Report the malaria status of this cell.
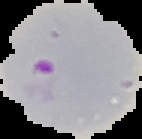

It is parasitized.

image type = segmented cell region with the area outside set to black
preparation = thin blood smear
image size = 142×139 pixels